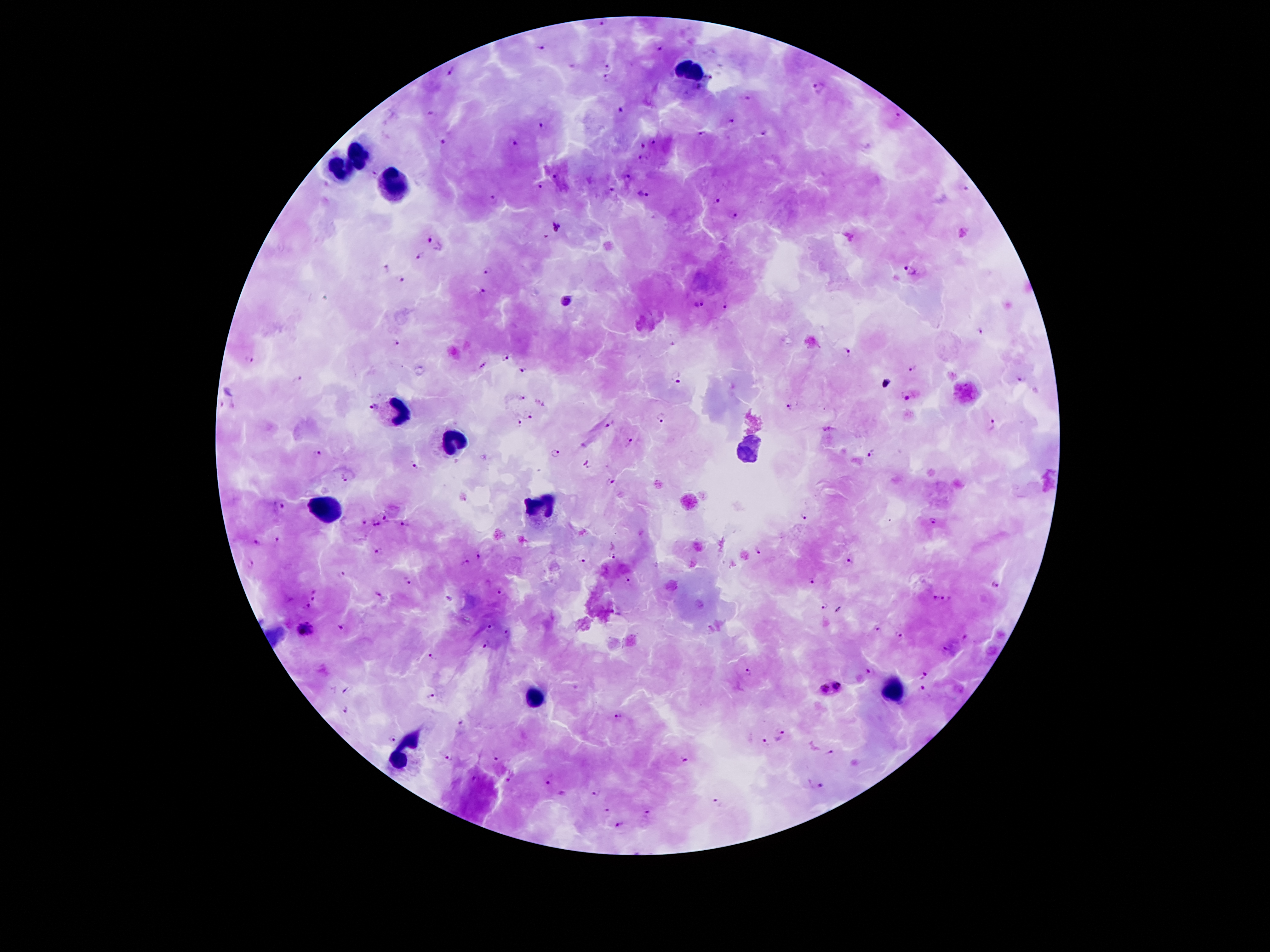
coordinate format = approximate centers as [x, y] in pixels
leukocyte locations = [692, 72], [358, 154], [339, 171], [394, 190], [398, 410], [453, 444], [750, 451], [541, 505], [327, 509], [893, 692], [539, 696], [404, 757]
malaria parasite locations = [603, 22], [540, 46], [661, 49], [572, 63], [608, 64], [450, 72], [606, 78], [709, 78], [818, 86], [748, 97], [621, 109], [432, 113], [897, 114], [730, 120], [543, 125], [763, 133], [702, 134], [443, 141], [513, 142], [656, 142], [644, 144], [642, 161], [556, 174], [627, 175], [539, 186], [963, 186], [612, 189], [644, 192], [494, 198], [717, 200], [734, 214], [557, 224], [434, 243], [420, 256], [386, 268], [908, 270], [488, 271], [400, 280], [483, 290], [566, 302], [700, 303], [725, 307], [980, 331], [397, 343], [848, 351], [505, 355], [248, 359], [913, 367], [524, 369], [676, 375], [1021, 377], [298, 379], [907, 397], [522, 398], [790, 404], [372, 406], [530, 416], [662, 418], [518, 423], [610, 424], [992, 425], [631, 440], [873, 452], [317, 453], [415, 464], [586, 464], [344, 478], [611, 482], [279, 505], [806, 516], [386, 519], [364, 521], [934, 521], [405, 522], [375, 523], [275, 539], [256, 542], [757, 550], [378, 552], [478, 554], [611, 555], [582, 560], [251, 562], [466, 563], [849, 563], [341, 573], [628, 578], [407, 579], [812, 579], [994, 587], [313, 593], [501, 593], [376, 594], [451, 597], [940, 598], [824, 604], [306, 607], [839, 610], [341, 626], [489, 628], [877, 628], [306, 631], [507, 632], [900, 635], [485, 644], [946, 650], [431, 655], [869, 669], [749, 672], [924, 676], [837, 686], [923, 687], [346, 691], [825, 692], [431, 696], [342, 709], [617, 716], [462, 724], [780, 734], [394, 737], [765, 744], [830, 753], [447, 757], [497, 760], [685, 760], [550, 780], [475, 781], [507, 781], [816, 786], [594, 791], [563, 794], [720, 800], [606, 812], [646, 815], [618, 824]
magnification = 100x
preparation = thick blood film
patient malaria status = infected with Plasmodium falciparum
capture = smartphone through the microscope eyepiece
field of view = one from this slide
stain = Giemsa
image size = 1270×952 pixels